Report the malaria status of this cell.
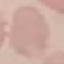
It is uninfected.

Summary:
  - Image type: cell patch, automatically extracted from a larger field of view and resized to 64 × 64 pixels
  - Capture: smartphone camera at the microscope eyepiece
  - Stain: Giemsa
  - Preparation: thin blood smear